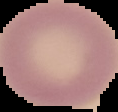

preparation = thin blood film
malaria status = uninfected
image size = 118×112 pixels
image type = cell region segmented out of the field of view; surrounding area masked to black